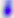

identification = Toxoplasma gondii
modality = photomicrograph
magnification = 400x